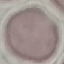
Summary:
  - Malaria status: uninfected
  - Preparation: thin blood film
  - Image type: automatically extracted cell patch, resized to 64 × 64 pixels
  - Capture: smartphone camera at the microscope eyepiece
  - Stain: Giemsa